Point out each Plasmodium parasite.
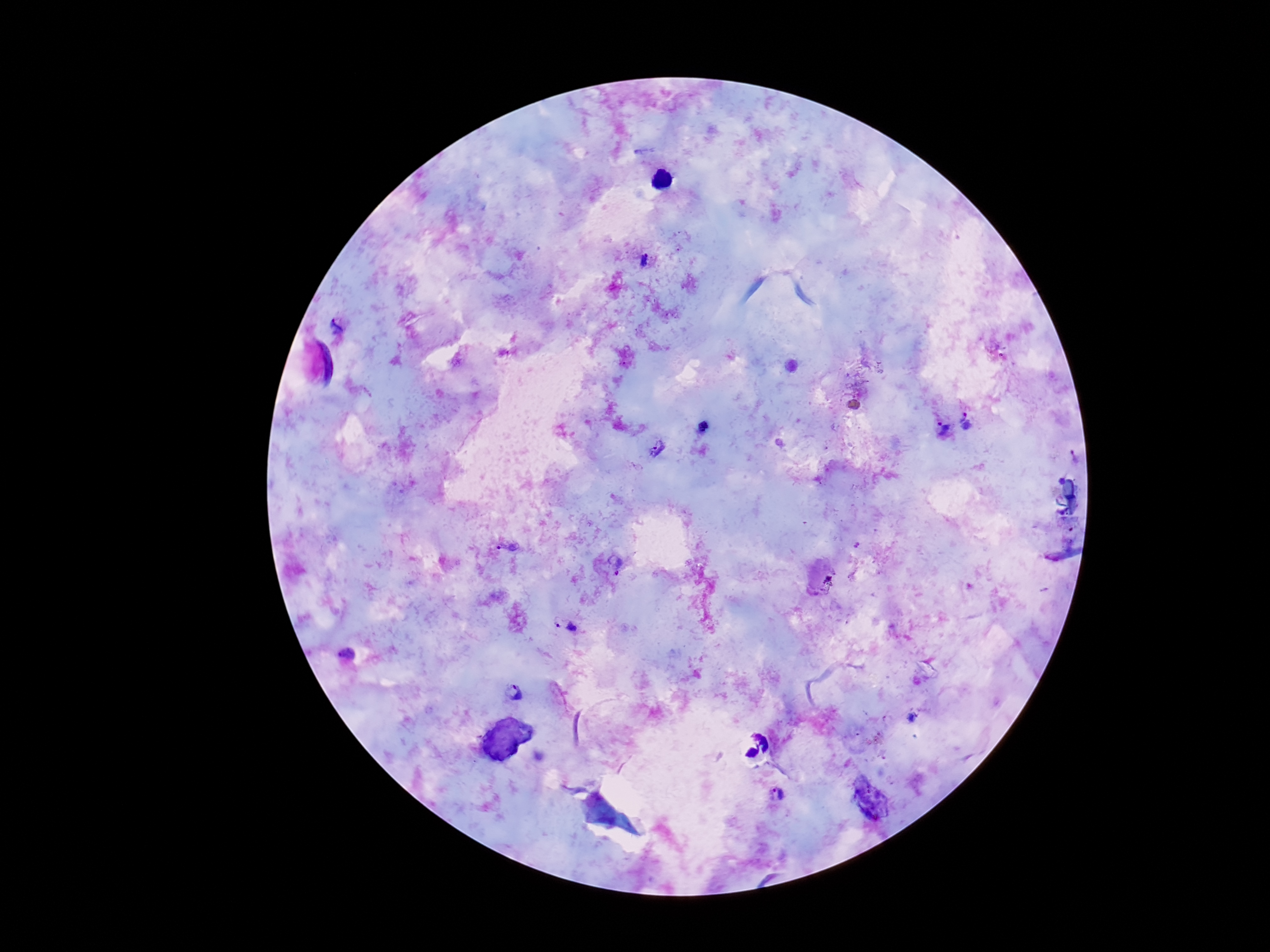
Approximate object centers, in pixels from the top-left corner.
Plasmodium parasites: (x=644, y=259), (x=339, y=326), (x=968, y=422), (x=943, y=430), (x=657, y=450), (x=509, y=546), (x=615, y=563), (x=823, y=575), (x=565, y=624), (x=346, y=654), (x=513, y=692), (x=777, y=794).

Summary:
  - Stain: Giemsa
  - Capture: smartphone camera through the microscope eyepiece
  - Preparation: thick peripheral-blood smear
  - Magnification: 100x
  - Field of view: single
  - Image size: 1270×952 pixels
  - Patient malaria status: infected